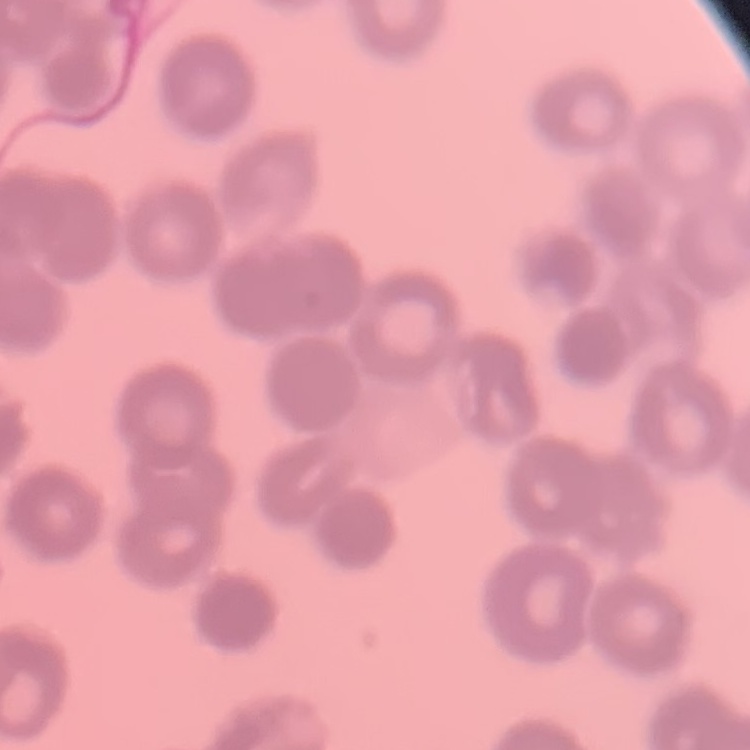

Summary:
  - Red blood cell morphology: rouleaux formation
  - Image type: square crop of a larger photomicrograph
  - Stain: Field's or Giemsa
  - Preparation: thin peripheral smear